Assess this cell for malaria.
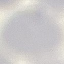
It is uninfected.

Photographed with a smartphone camera at the microscope eyepiece. Thin blood smear. Giemsa stain. Automatically extracted cell patch, resized to 64 × 64 pixels.